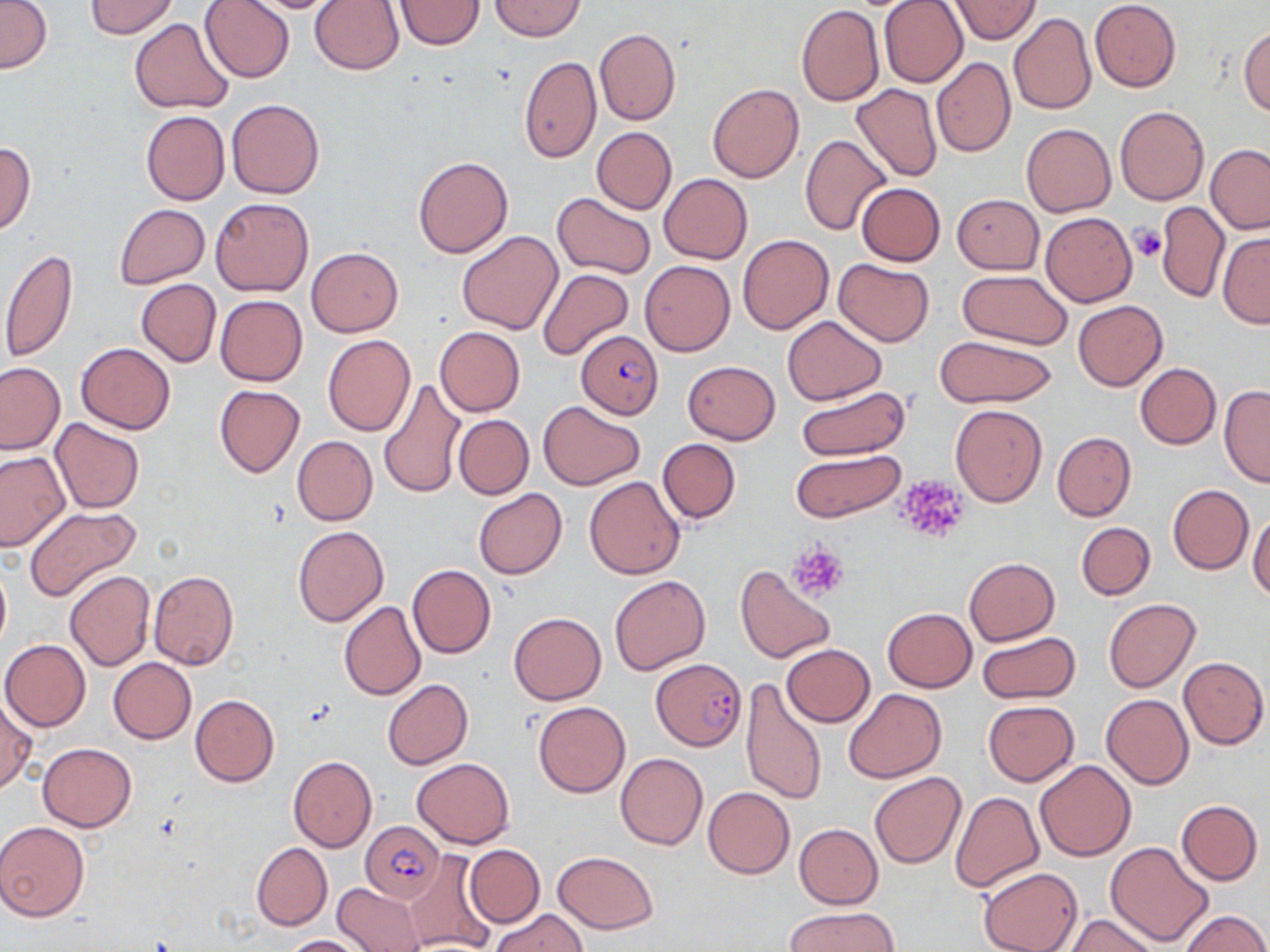

Approximate bounding boxes as (x1, y1, x2, y2) in pixels. Plasmodium falciparum-infected red blood cell locations: (576, 329, 664, 419), (651, 658, 748, 750), (360, 822, 444, 901). Platelet locations: (1128, 225, 1167, 263), (893, 473, 972, 545), (787, 540, 849, 601). Uninfected red blood cell locations: (86, 0, 180, 38), (199, 0, 295, 84), (949, 0, 1041, 44), (1089, 0, 1181, 92), (1, 1, 52, 73), (235, 1, 351, 13), (310, 1, 404, 74), (394, 1, 484, 50), (490, 1, 585, 40), (880, 1, 968, 87), (796, 4, 884, 105), (1009, 13, 1097, 116), (130, 19, 236, 115), (1239, 25, 1269, 116), (594, 27, 681, 125), (519, 57, 601, 163), (931, 57, 1016, 158), (888, 77, 1004, 177), (708, 82, 805, 183), (851, 83, 942, 182), (226, 99, 324, 198), (1115, 106, 1209, 205), (141, 110, 230, 205), (1021, 123, 1115, 216), (592, 127, 677, 215), (800, 134, 892, 236), (0, 141, 36, 235), (1206, 144, 1270, 233), (413, 156, 513, 258), (659, 174, 753, 263), (856, 183, 945, 265), (553, 192, 656, 279), (952, 194, 1044, 274), (211, 197, 313, 296), (1156, 199, 1229, 303), (114, 203, 209, 290), (1040, 211, 1137, 306), (457, 230, 562, 335), (1218, 233, 1270, 328), (737, 234, 834, 334), (306, 247, 403, 336), (2, 249, 76, 364), (833, 258, 934, 346), (639, 260, 735, 356), (538, 270, 634, 360), (957, 270, 1072, 350), (136, 279, 221, 367), (215, 295, 307, 386), (1073, 300, 1168, 390), (782, 316, 886, 404), (435, 326, 525, 416), (935, 334, 1055, 407), (322, 335, 416, 436), (76, 343, 175, 433), (682, 361, 781, 444), (0, 362, 64, 454), (1135, 363, 1221, 449), (378, 379, 465, 500), (796, 385, 911, 461), (1219, 385, 1270, 487), (214, 386, 305, 477), (537, 399, 645, 490), (949, 404, 1047, 508), (454, 415, 534, 499), (51, 418, 145, 514), (1052, 432, 1136, 520), (292, 435, 377, 525), (658, 438, 741, 524), (792, 449, 905, 522), (0, 451, 68, 551), (584, 476, 685, 579), (1168, 484, 1253, 574), (473, 488, 566, 580), (24, 507, 141, 599), (1248, 510, 1270, 601), (1076, 522, 1155, 600), (293, 526, 389, 627), (0, 557, 11, 653), (963, 557, 1060, 644), (406, 564, 495, 658), (735, 564, 836, 664), (65, 570, 155, 671), (148, 570, 239, 670), (610, 575, 711, 675), (1103, 598, 1200, 692), (339, 602, 426, 700), (882, 608, 976, 691), (509, 613, 606, 705), (976, 631, 1080, 702), (1, 639, 90, 732), (781, 644, 875, 727), (1178, 656, 1268, 748), (109, 658, 197, 743), (381, 679, 474, 770), (738, 681, 828, 806), (843, 688, 946, 783), (1101, 694, 1193, 789), (190, 695, 278, 786), (0, 698, 35, 795), (533, 701, 630, 797), (983, 701, 1079, 785), (37, 743, 137, 832), (615, 752, 708, 850), (288, 756, 378, 853), (412, 758, 515, 848), (1035, 760, 1135, 862), (868, 772, 966, 869), (703, 786, 795, 878), (948, 792, 1043, 893), (1176, 799, 1262, 885), (0, 821, 90, 921), (794, 824, 883, 909), (1105, 841, 1214, 946), (251, 842, 332, 930), (464, 844, 544, 927), (404, 850, 498, 952), (553, 850, 658, 933), (978, 866, 1083, 952), (333, 883, 424, 951), (787, 905, 900, 951), (491, 909, 588, 951), (1179, 909, 1268, 952), (1064, 912, 1160, 952), (282, 934, 370, 952). Slide-level diagnosis: Plasmodium falciparum. Image is 1270×952 pixels. Light microscopy. Thin blood smear. Single field of view. May-Grünwald-Giemsa stain. Captured at 1000x magnification.